Outline each blood parasite and name the species.
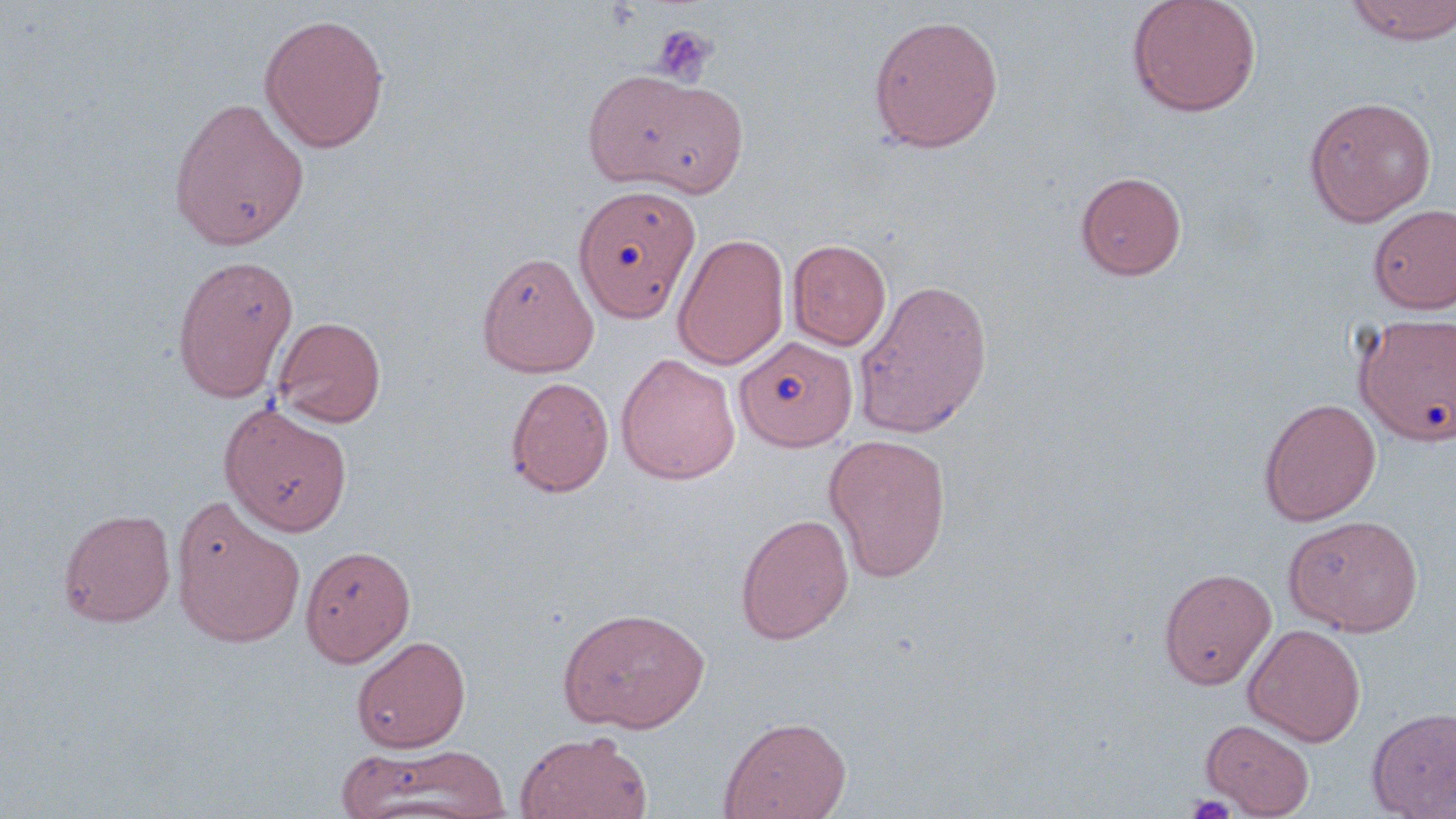

No blood parasites observed.

Summary:
  - Coordinate format: approximate bounding boxes as [x1, y1, x2, y2] in pixels
  - Platelet locations: [650, 23, 718, 86], [1185, 793, 1237, 819]
  - Uninfected red blood cell locations: [1126, 0, 1263, 118], [1345, 0, 1456, 45], [258, 13, 390, 154], [868, 13, 1004, 153], [582, 69, 713, 189], [629, 81, 750, 198], [1303, 95, 1437, 226], [168, 96, 310, 251], [1075, 171, 1186, 279], [573, 183, 701, 322], [1368, 204, 1456, 314], [672, 232, 790, 371], [787, 239, 892, 350], [476, 250, 599, 378], [171, 254, 299, 403], [852, 277, 994, 439], [1354, 312, 1455, 446], [272, 316, 386, 427], [735, 336, 857, 450], [615, 352, 741, 485], [505, 375, 615, 497], [1259, 397, 1381, 526], [219, 403, 353, 536], [823, 433, 952, 582], [171, 498, 306, 649], [58, 508, 176, 628], [735, 512, 855, 644], [1283, 514, 1423, 636], [300, 544, 416, 667], [1158, 567, 1276, 689], [556, 605, 711, 734], [1243, 624, 1366, 746], [351, 634, 471, 753], [1366, 706, 1456, 818], [719, 715, 851, 819], [1201, 718, 1315, 817], [515, 731, 653, 819], [337, 741, 512, 819]
  - Slide-level diagnosis: no evidence of blood parasites
  - Stain: May-Grünwald-Giemsa
  - Field of view: one of a larger specimen
  - Magnification: 1000x
  - Image size: 1456×819 pixels
  - Modality: light microscopy
  - Preparation: thin blood smear